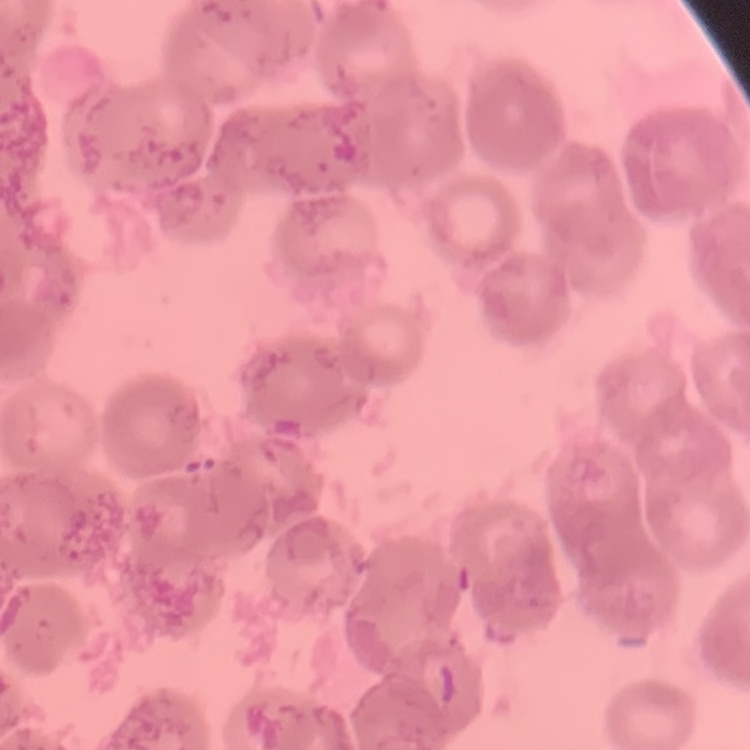
erythrocyte_morphology: rouleaux formation
preparation: thin blood smear
stain: Field's or Giemsa
image_type: square crop of a larger photomicrograph